Classify this cell by malaria status.
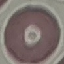

It is uninfected.

preparation = thin smear
image type = automatically extracted cell patch, resized to 64 × 64 pixels
capture = smartphone camera at the microscope eyepiece
stain = Giemsa